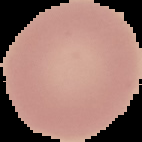

Summary:
  - Preparation: thin blood smear
  - Image size: 142×142 pixels
  - Image type: segmented cell region on a black background
  - Result: negative for malaria parasites